Name the cell type shown.
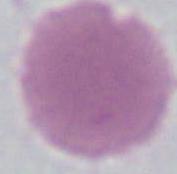
An erythrocyte.

Summary:
  - Modality: micrograph
  - Magnification: 1000x